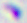
Photomicrograph. Toxoplasma gondii is seen. Captured at 400x magnification.